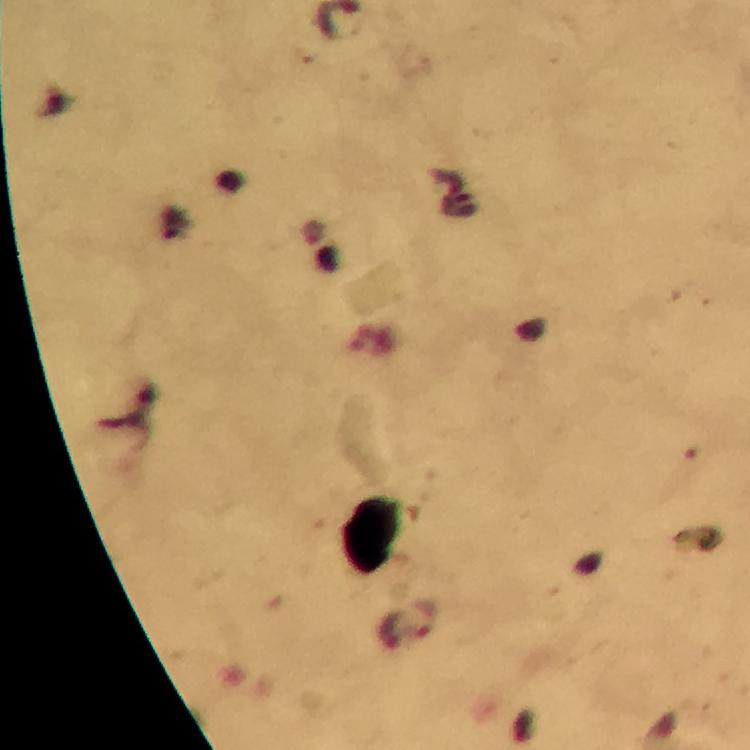

Approximate centers as {x, y} in pixels.
Summary:
  - Malaria parasite locations: {427, 618}
  - Cropped from: one field of view
  - Magnification: 100x
  - Image size: 750×750 pixels
  - Immersion oil: used
  - Preparation: thick blood smear
  - Context: from a malaria diagnostic workup
  - Capture: smartphone camera through the microscope
  - Stain: Giemsa